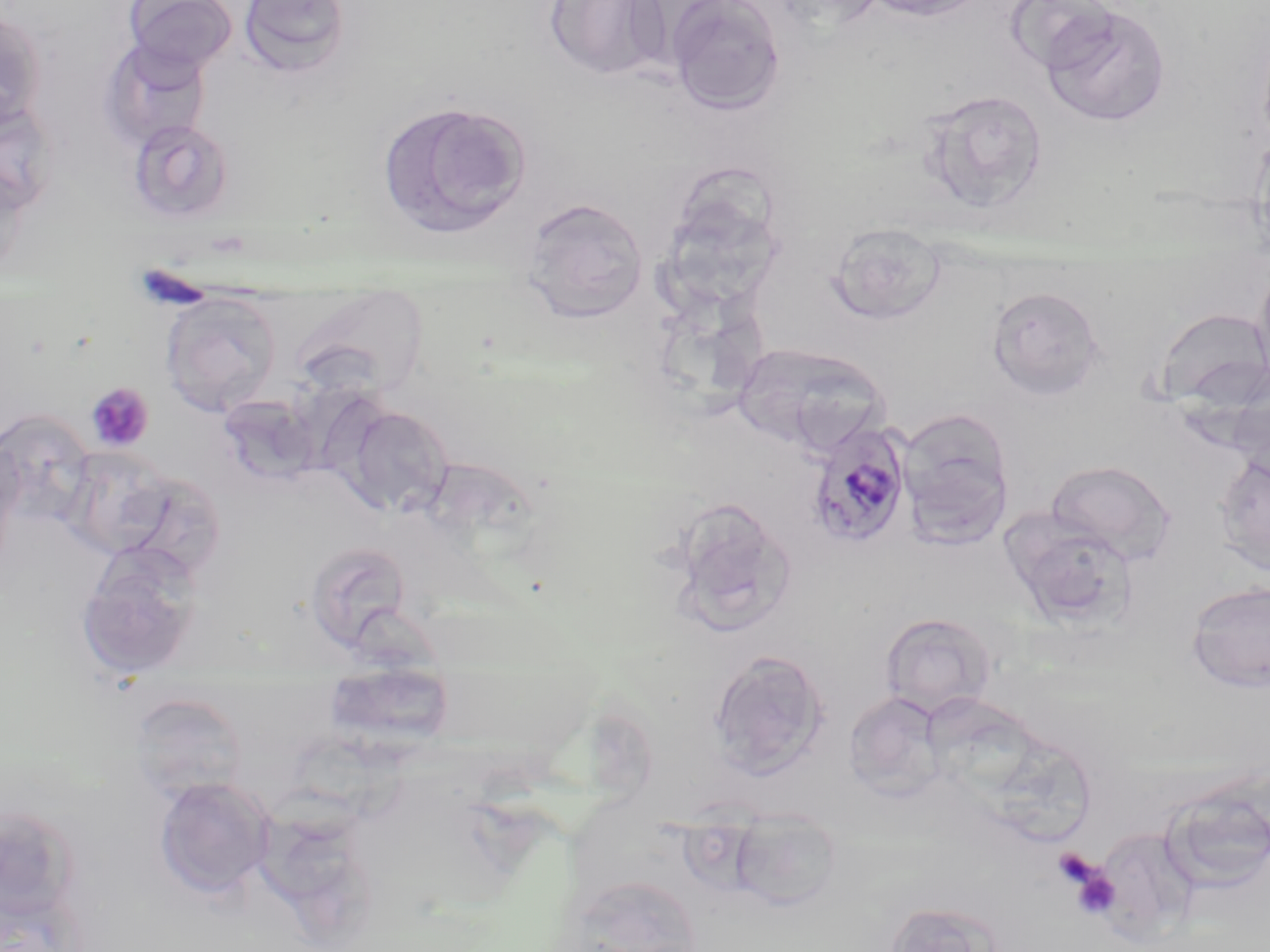
Summary:
  - Coordinate format: approximate bounding boxes as [x1, y1, x2, y2] in pixels
  - Platelet locations: [132, 263, 215, 310], [87, 383, 154, 452], [1052, 848, 1096, 886], [1070, 866, 1121, 919]
  - Plasmodium malariae-infected red blood cell locations: [804, 419, 914, 550]
  - Uninfected red blood cell locations: [124, 0, 238, 75], [237, 0, 353, 78], [544, 0, 668, 81], [770, 0, 886, 31], [861, 0, 988, 21], [1006, 0, 1117, 75], [667, 1, 786, 115], [1040, 4, 1172, 128], [0, 10, 47, 130], [99, 39, 212, 149], [917, 88, 1049, 214], [0, 99, 60, 213], [376, 100, 532, 240], [127, 118, 236, 225], [1252, 131, 1270, 262], [0, 158, 32, 280], [520, 197, 649, 323], [828, 222, 946, 325], [1252, 259, 1270, 389], [986, 285, 1106, 401], [291, 290, 429, 398], [160, 293, 282, 417], [1155, 307, 1270, 410], [733, 342, 886, 455], [1226, 379, 1270, 482], [343, 405, 454, 517], [898, 407, 1015, 542], [0, 411, 96, 525], [0, 438, 26, 560], [63, 447, 172, 558], [1213, 454, 1270, 576], [1045, 459, 1175, 563], [114, 470, 229, 583], [668, 497, 797, 637], [1001, 509, 1137, 630], [76, 541, 204, 680], [304, 541, 413, 653], [1185, 580, 1270, 694], [879, 612, 997, 718], [708, 649, 830, 777], [324, 661, 454, 751], [843, 691, 947, 800], [128, 692, 250, 801], [153, 775, 275, 901], [729, 807, 844, 912], [567, 873, 702, 951], [884, 899, 1006, 952]
  - Slide-level diagnosis: Plasmodium malariae
  - Field of view: one of a larger specimen
  - Magnification: 1000x
  - Modality: optical microscopy
  - Image size: 1270×952 pixels
  - Preparation: thin blood film
  - Stain: May-Grünwald-Giemsa